Locate every Plasmodium falciparum-infected red blood cell.
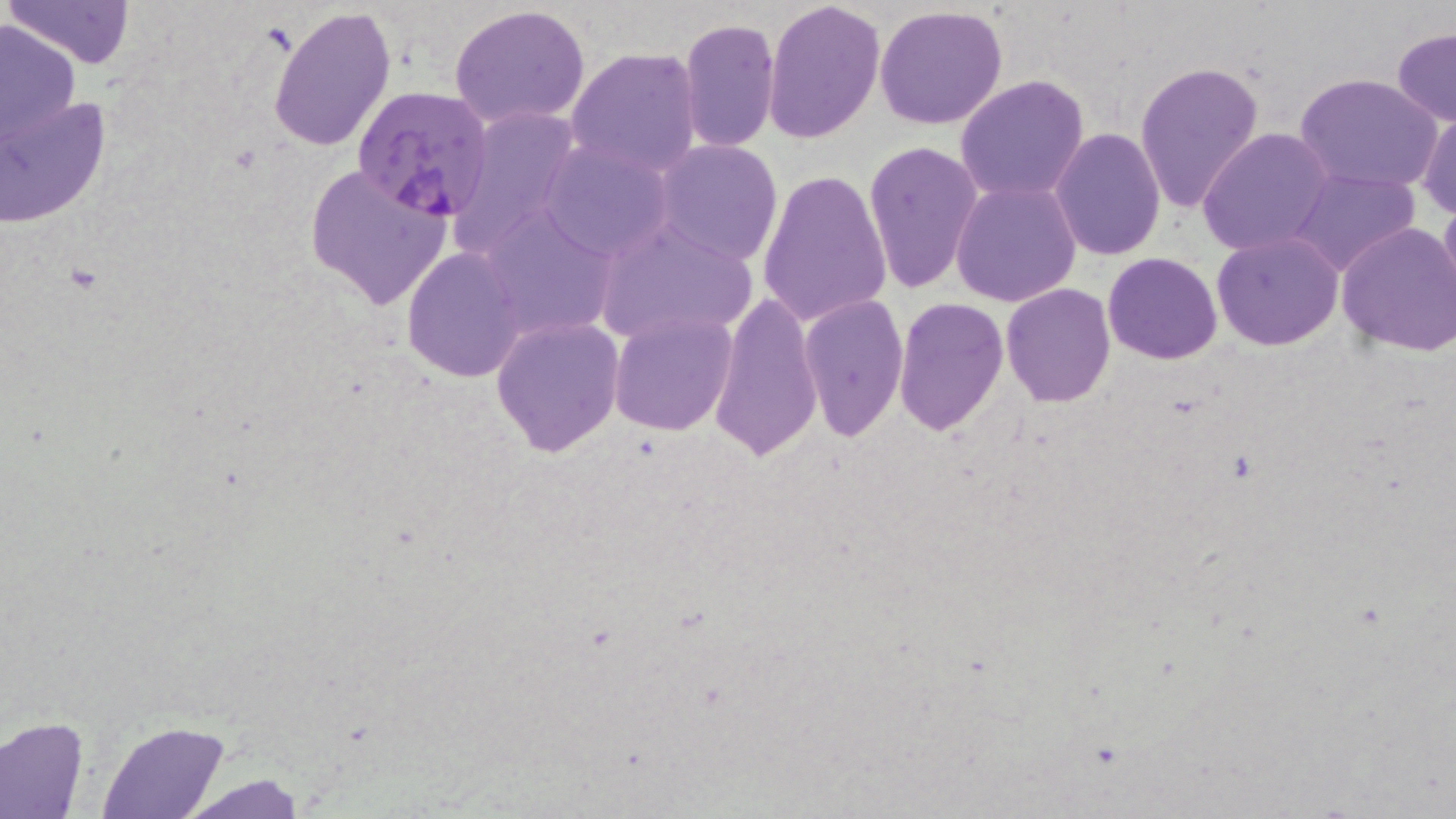

Approximate bounding boxes as named x1/y1/x2/y2 corners in pixels.
Plasmodium falciparum-infected red blood cells: (x1=353, y1=87, x2=495, y2=221).

Uninfected red blood cell locations: (x1=4, y1=0, x2=134, y2=71), (x1=764, y1=0, x2=885, y2=146), (x1=267, y1=4, x2=398, y2=154), (x1=447, y1=5, x2=592, y2=132), (x1=875, y1=6, x2=1009, y2=129), (x1=0, y1=16, x2=81, y2=157), (x1=678, y1=17, x2=780, y2=152), (x1=1390, y1=29, x2=1455, y2=126), (x1=565, y1=47, x2=703, y2=177), (x1=1133, y1=59, x2=1265, y2=216), (x1=3, y1=70, x2=110, y2=234), (x1=1295, y1=72, x2=1444, y2=195), (x1=955, y1=73, x2=1089, y2=204), (x1=449, y1=105, x2=585, y2=252), (x1=1418, y1=109, x2=1456, y2=221), (x1=1052, y1=128, x2=1165, y2=260), (x1=1197, y1=128, x2=1333, y2=258), (x1=864, y1=138, x2=982, y2=294), (x1=539, y1=140, x2=672, y2=261), (x1=654, y1=140, x2=782, y2=264), (x1=303, y1=163, x2=454, y2=311), (x1=1288, y1=168, x2=1420, y2=277), (x1=757, y1=171, x2=891, y2=327), (x1=951, y1=178, x2=1080, y2=306), (x1=1439, y1=189, x2=1456, y2=310), (x1=473, y1=204, x2=617, y2=341), (x1=593, y1=218, x2=759, y2=349), (x1=1335, y1=222, x2=1456, y2=357), (x1=1212, y1=231, x2=1343, y2=350), (x1=402, y1=247, x2=526, y2=381), (x1=1102, y1=252, x2=1223, y2=364), (x1=1003, y1=282, x2=1114, y2=405), (x1=707, y1=290, x2=822, y2=462), (x1=798, y1=294, x2=907, y2=440), (x1=895, y1=296, x2=1008, y2=436), (x1=610, y1=311, x2=736, y2=435), (x1=491, y1=315, x2=624, y2=457), (x1=0, y1=717, x2=89, y2=818), (x1=95, y1=721, x2=231, y2=818), (x1=178, y1=776, x2=311, y2=816). Slide-level diagnosis: Plasmodium falciparum. One field of a larger specimen. Image is 1456×819 pixels. Thin blood film. Captured at 1000x magnification. May-Grünwald-Giemsa-stained preparation. Light microscopy.